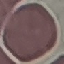
{
  "malaria_status": "uninfected",
  "image_type": "cell patch, automatically extracted from a larger field of view and resized to 64 × 64 pixels",
  "stain": "Giemsa",
  "preparation": "thin smear",
  "capture": "smartphone through the microscope eyepiece"
}